Identify the blood parasite species.
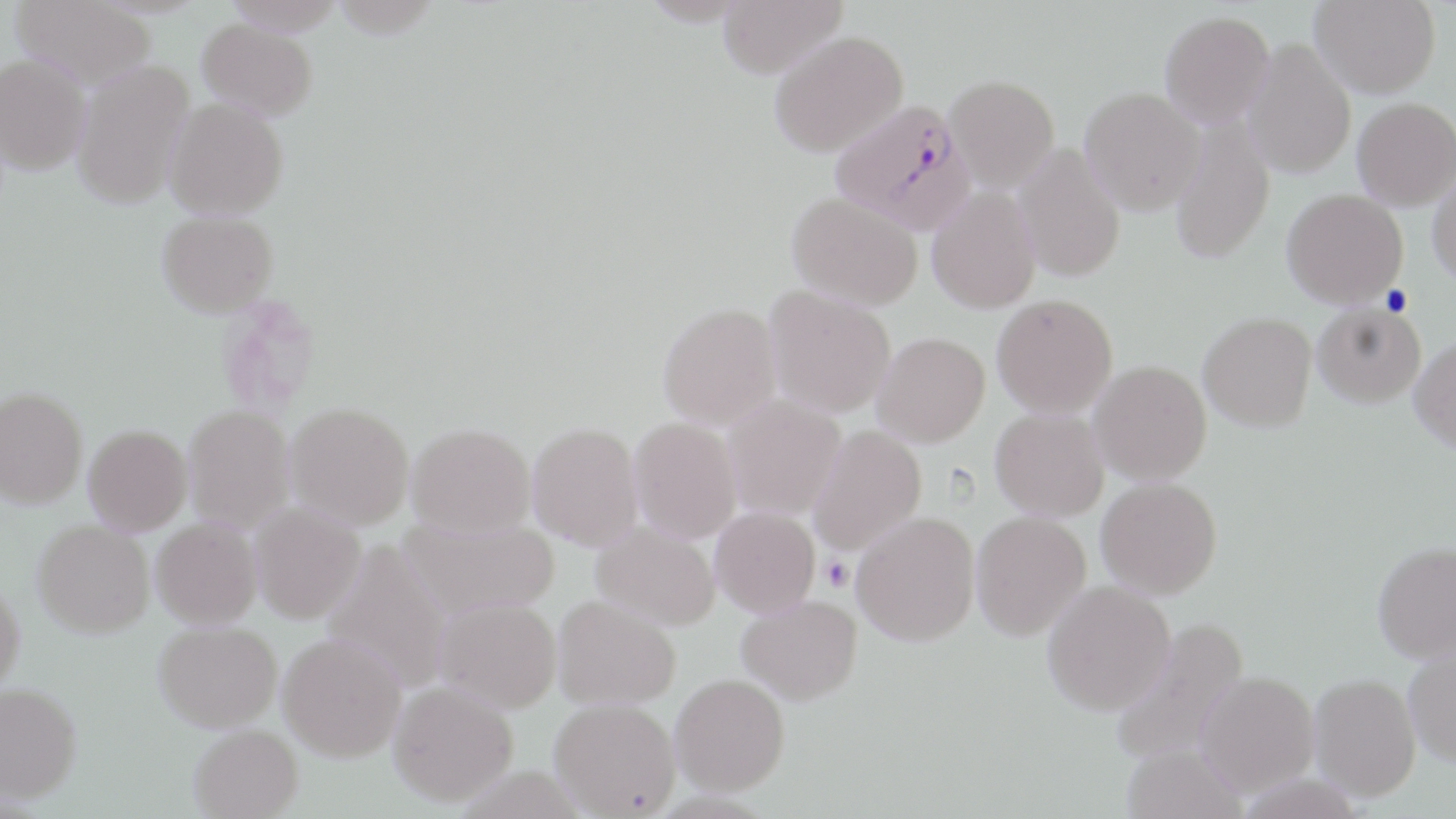
Plasmodium falciparum.

Approximate bounding boxes as (x1, y1, x2, y2) in pixels. Uninfected red blood cell locations: (10, 0, 158, 90), (223, 0, 345, 36), (638, 0, 756, 26), (717, 0, 846, 78), (1310, 0, 1441, 98), (1160, 11, 1275, 128), (198, 18, 317, 119), (769, 30, 908, 157), (1243, 38, 1356, 179), (0, 53, 91, 175), (71, 59, 194, 210), (944, 75, 1059, 191), (1080, 86, 1204, 215), (164, 97, 288, 220), (1352, 97, 1456, 209), (1170, 115, 1274, 265), (1013, 143, 1126, 283), (1429, 166, 1456, 287), (927, 186, 1041, 314), (1282, 188, 1407, 308), (788, 192, 922, 310), (156, 210, 279, 316), (764, 285, 896, 418), (992, 293, 1117, 417), (658, 302, 781, 429), (1313, 303, 1426, 407), (1198, 312, 1317, 431), (873, 332, 990, 446), (1410, 336, 1456, 452), (1090, 360, 1212, 484), (0, 387, 87, 508), (722, 395, 846, 520), (285, 402, 414, 529), (183, 404, 295, 534), (990, 408, 1108, 520), (629, 418, 741, 544), (528, 422, 642, 550), (407, 423, 534, 535), (83, 425, 192, 535), (809, 425, 926, 554), (1097, 477, 1222, 599), (249, 502, 366, 624), (710, 506, 820, 618), (851, 511, 980, 646), (970, 511, 1091, 641), (151, 517, 263, 628), (397, 517, 559, 621), (33, 520, 154, 638), (591, 521, 720, 630), (321, 539, 455, 693), (1372, 541, 1456, 663), (0, 578, 25, 699), (1042, 580, 1176, 715), (552, 595, 680, 711), (736, 595, 863, 705), (434, 597, 561, 713), (1109, 618, 1250, 768), (154, 621, 282, 732), (279, 633, 406, 761), (1403, 643, 1456, 767), (1195, 671, 1319, 795), (670, 673, 790, 795), (1309, 673, 1420, 800), (388, 681, 518, 806), (0, 682, 82, 803), (549, 698, 680, 817), (189, 724, 302, 818), (1120, 743, 1246, 819). Plasmodium falciparum-infected red blood cell locations: (830, 98, 974, 234). Platelet locations: (1380, 285, 1413, 316), (820, 556, 853, 590). One field of a larger specimen. Light microscopy. Captured at 1000x magnification. Thin blood film. May-Grünwald-Giemsa-stained preparation. Image is 1456×819 pixels.